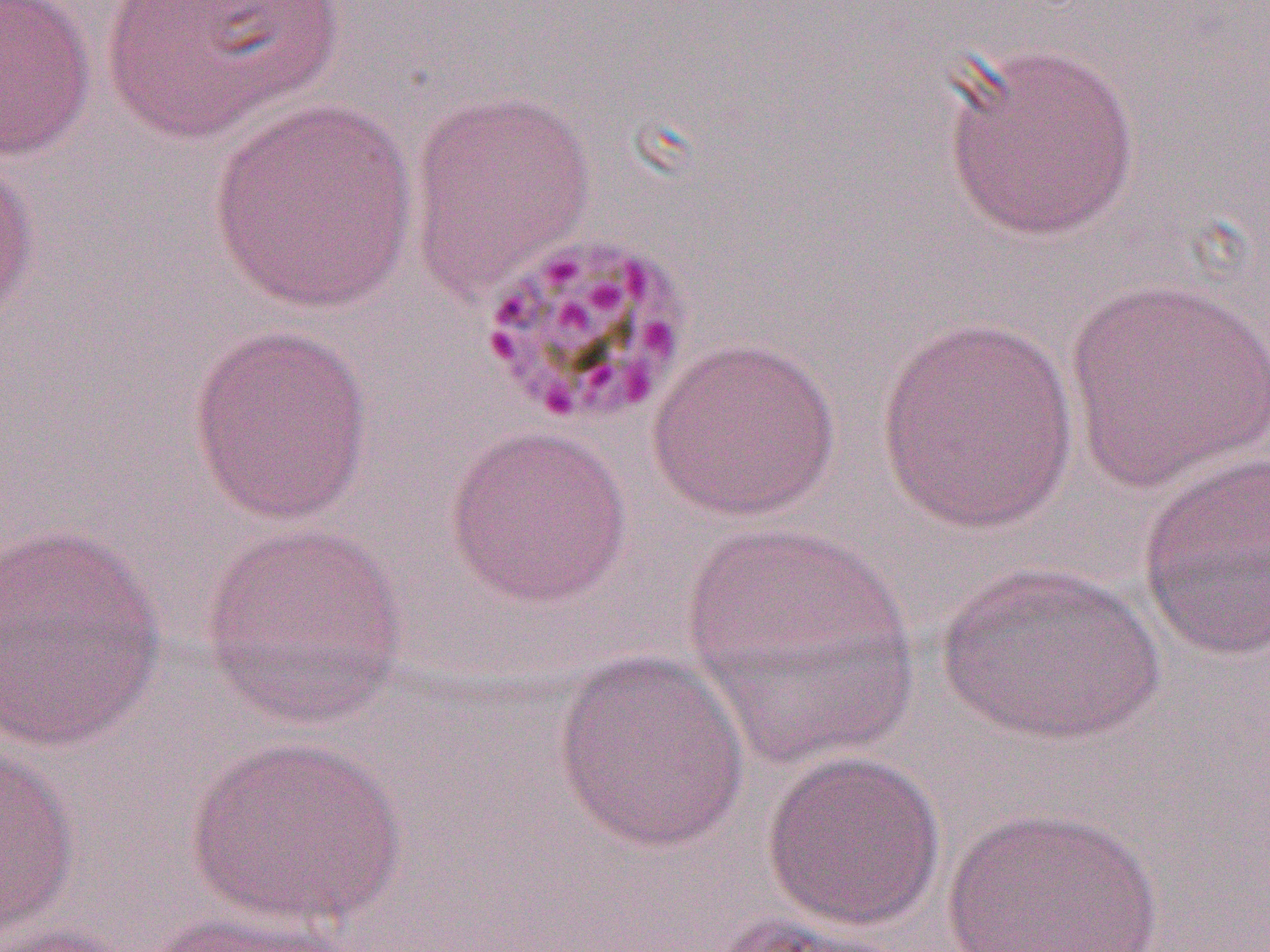

slide_level_diagnosis: Plasmodium malariae
image_size: 1270×952 pixels
field_of_view: one of a larger specimen
modality: optical microscopy
uninfected_red_blood_cell_locations: 'approximate bounding boxes as (x1, y1, x2, y2) in pixels: (0, 0, 96, 161), (97, 0, 349, 144), (939, 41, 1143, 242), (406, 86, 597, 298), (206, 99, 418, 314), (0, 154, 40, 332), (1063, 275, 1270, 497), (873, 317, 1081, 534), (186, 323, 375, 526), (647, 337, 840, 522), (444, 423, 634, 609), (1137, 450, 1270, 662), (679, 518, 920, 767), (199, 522, 410, 729), (0, 524, 168, 754), (937, 559, 1165, 747), (552, 651, 751, 855), (184, 734, 408, 927), (0, 746, 80, 941), (760, 747, 948, 931), (941, 804, 1166, 952), (137, 907, 361, 952), (700, 911, 910, 951), (1, 922, 142, 952)'
magnification: 1000x
preparation: thin blood film